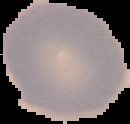
Result: no malaria parasites seen. Image is 130×124 pixels. From a thin blood smear. Segmented cell region on a black background.